Assess this cell for malaria.
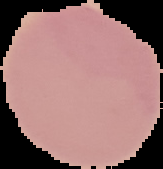
It is uninfected.

Cell region segmented out of the field of view; the surrounding area is masked to black. From a thin blood smear. Image is 163×169 pixels.